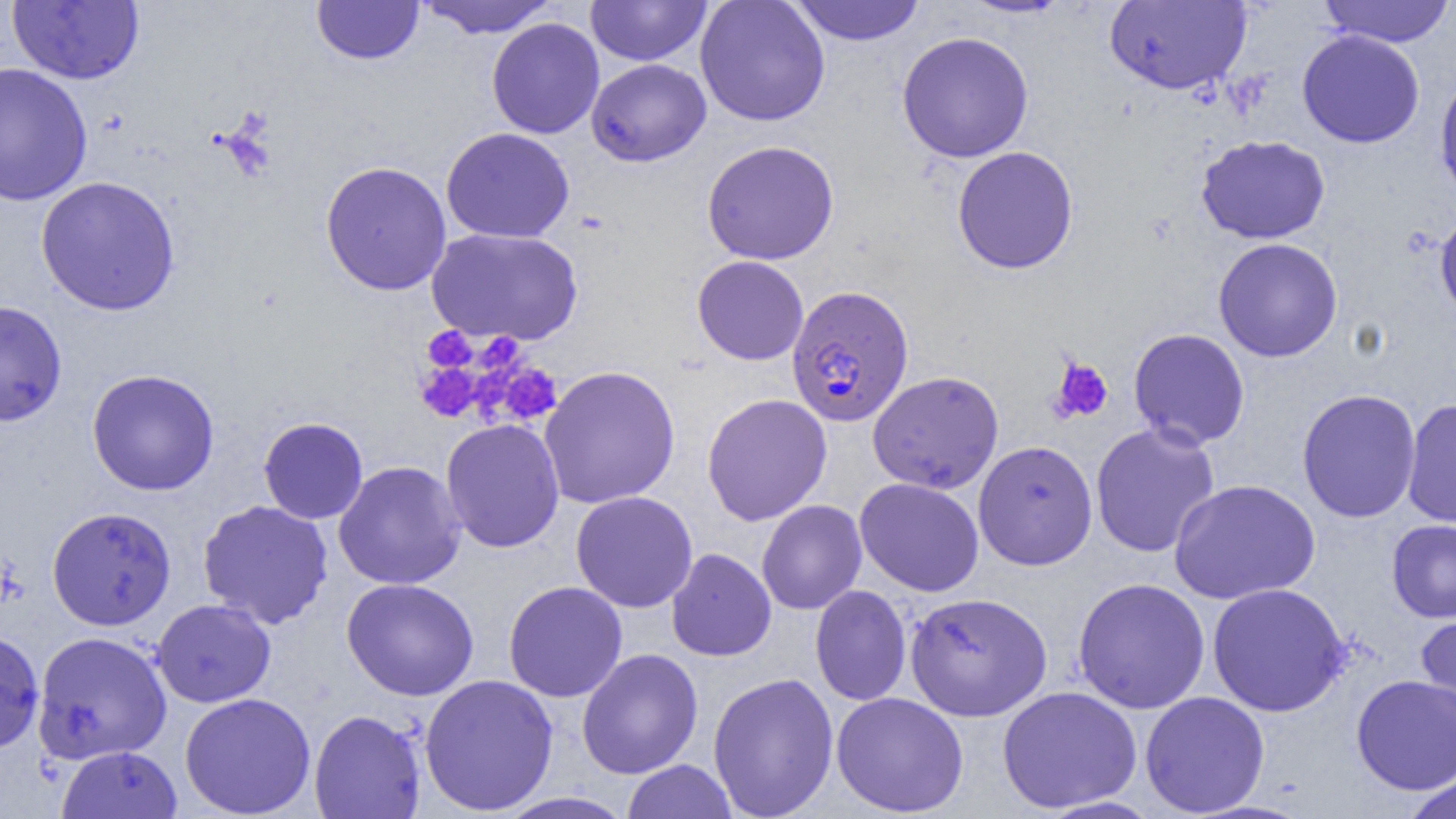
Approximate bounding boxes as (x1, y1, x2, y2) in pixels. Plasmodium falciparum-infected red blood cell locations: (786, 284, 914, 428). Platelet locations: (422, 327, 477, 372), (475, 333, 525, 377), (1048, 357, 1113, 424), (415, 362, 481, 422), (488, 362, 564, 426). Uninfected red blood cell locations: (419, 0, 559, 38), (585, 0, 713, 66), (788, 0, 927, 45), (959, 0, 1074, 18), (1104, 0, 1253, 95), (1318, 0, 1455, 47), (7, 1, 144, 85), (311, 1, 425, 65), (695, 1, 830, 126), (486, 18, 604, 139), (1297, 30, 1425, 148), (896, 31, 1034, 163), (586, 58, 712, 167), (0, 61, 93, 206), (1434, 69, 1456, 204), (441, 127, 575, 244), (1196, 135, 1330, 244), (701, 140, 840, 265), (952, 146, 1079, 274), (320, 160, 452, 296), (35, 176, 181, 315), (1435, 208, 1456, 323), (427, 227, 583, 345), (1213, 238, 1343, 362), (692, 255, 809, 365), (0, 299, 67, 427), (1128, 328, 1250, 449), (539, 365, 681, 509), (87, 369, 220, 496), (867, 370, 1004, 494), (1296, 389, 1421, 523), (702, 393, 832, 525), (1401, 398, 1456, 528), (258, 417, 369, 524), (441, 419, 565, 553), (1090, 422, 1220, 558), (973, 440, 1098, 571), (333, 461, 466, 589), (855, 478, 984, 596), (1167, 479, 1322, 605), (570, 491, 698, 613), (196, 499, 334, 629), (756, 499, 867, 615), (47, 506, 177, 631), (1386, 519, 1456, 623), (666, 548, 776, 662), (341, 577, 479, 701), (1072, 577, 1210, 714), (503, 581, 628, 702), (1207, 582, 1351, 717), (810, 585, 912, 706), (905, 591, 1052, 721), (152, 599, 276, 708), (1415, 612, 1456, 723), (0, 628, 45, 753), (32, 630, 172, 764), (576, 648, 703, 779), (708, 671, 839, 818), (419, 673, 558, 815), (1351, 674, 1456, 795), (997, 686, 1142, 814), (179, 691, 316, 818), (831, 691, 969, 817), (1139, 691, 1270, 817), (309, 709, 427, 819), (56, 745, 182, 819), (622, 759, 738, 818), (1400, 768, 1456, 819), (493, 791, 637, 819). Slide-level diagnosis: Plasmodium falciparum. Image is 1456×819 pixels. Captured at 1000x magnification. Optical microscopy. Thin blood film. One field of a larger specimen.